Describe the morphology of the erythrocytes.
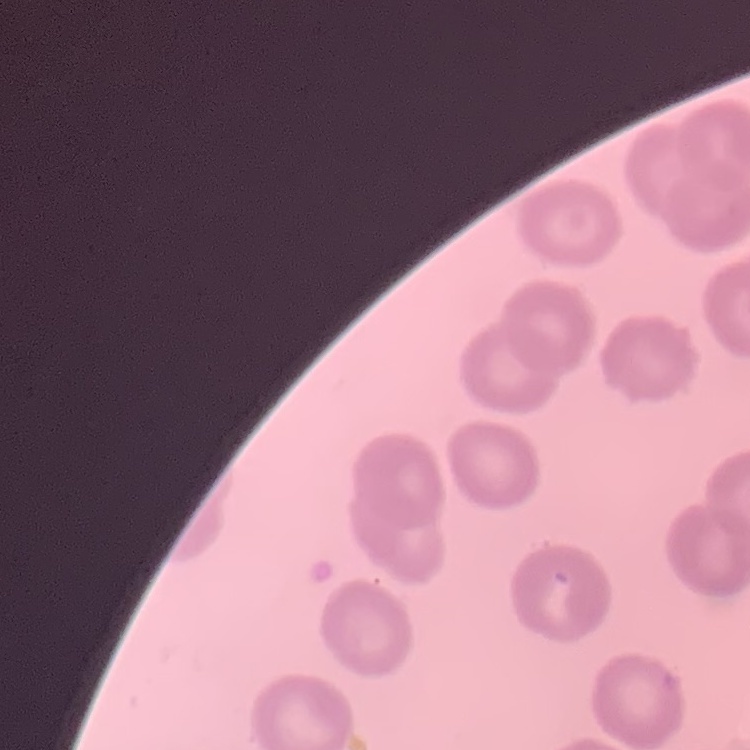

No rouleaux formation.

Thin blood film. Stained with either Field's or Giemsa. Square crop of a larger photomicrograph.